Report the malaria status of this cell.
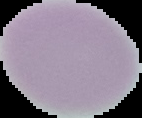
It is uninfected.

image type = cell region segmented out of the field of view; surrounding area masked to black
preparation = thin blood film
image size = 142×118 pixels